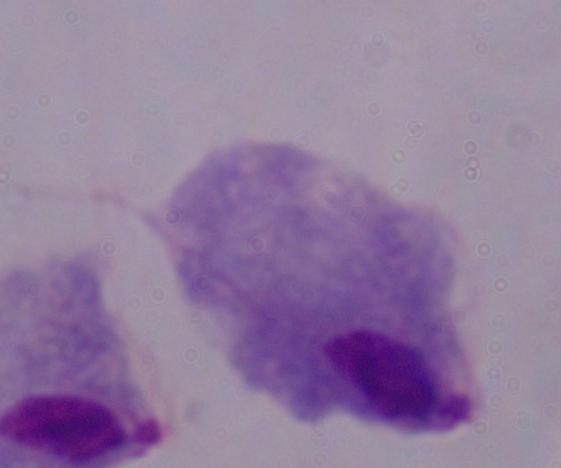
1000x magnification. Photomicrograph. A trichomonad is seen.